Assess this cell for malaria.
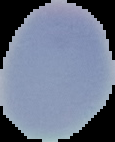
It is uninfected.

Summary:
  - Image size: 115×142 pixels
  - Preparation: thin blood film
  - Image type: segmented cell region with the area outside set to black